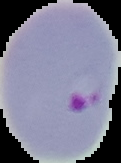

malaria status = parasitized
preparation = thin blood smear
image size = 121×163 pixels
image type = segmented cell region on a black background